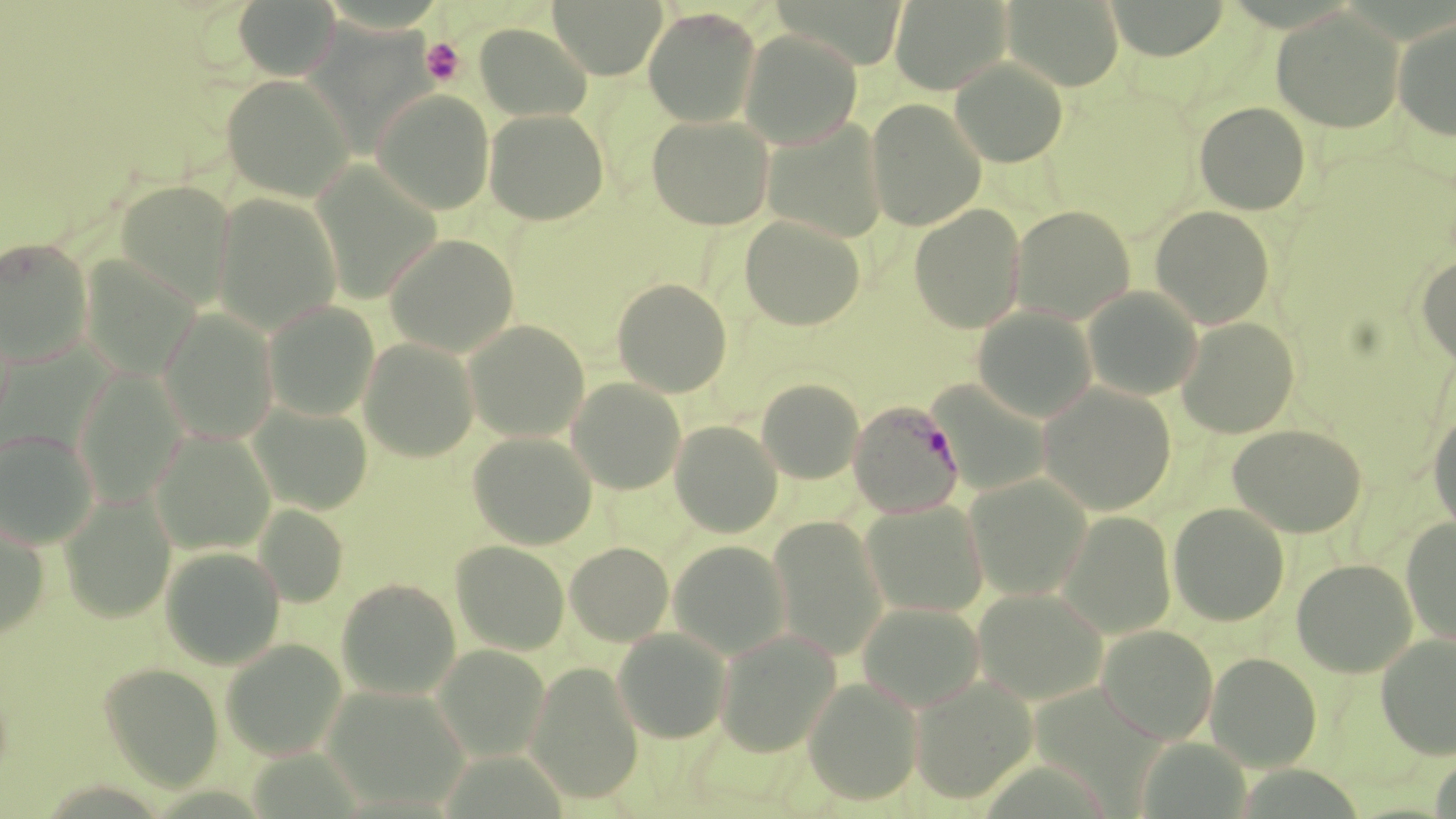
slide-level diagnosis = Plasmodium malariae
stain = May-Grünwald-Giemsa
Plasmodium malariae-infected red blood cell locations = approximate bounding boxes as [x1, y1, x2, y2] in pixels: [848, 400, 964, 518]
field of view = single
magnification = 1000x
modality = optical microscopy
platelet locations = approximate bounding boxes as [x1, y1, x2, y2] in pixels: [421, 38, 465, 86]
image size = 1456×819 pixels
preparation = thin blood film
uninfected red blood cell locations = approximate bounding boxes as [x1, y1, x2, y2] in pixels: [233, 0, 339, 80], [549, 0, 666, 79], [1003, 0, 1125, 90], [1104, 0, 1230, 60], [889, 1, 1011, 95], [643, 7, 762, 128], [1272, 8, 1404, 133], [303, 10, 442, 145], [1393, 16, 1456, 141], [475, 23, 592, 121], [739, 29, 862, 149], [951, 58, 1068, 167], [221, 74, 354, 201], [372, 89, 495, 215], [866, 99, 986, 231], [1194, 102, 1311, 214], [485, 108, 609, 225], [646, 115, 774, 230], [761, 119, 889, 244], [310, 162, 442, 305], [114, 180, 236, 309], [212, 193, 342, 334], [909, 204, 1026, 334], [1010, 205, 1135, 323], [1150, 206, 1275, 329], [739, 214, 866, 331], [385, 233, 520, 357], [0, 237, 94, 366], [1416, 255, 1456, 370], [77, 257, 201, 381], [612, 278, 732, 397], [1082, 286, 1203, 401], [263, 301, 380, 421], [973, 306, 1098, 423], [158, 309, 279, 444], [1176, 316, 1299, 438], [464, 320, 590, 442], [358, 337, 480, 462], [73, 368, 188, 507], [567, 378, 686, 494], [757, 378, 864, 484], [928, 381, 1052, 496], [1038, 384, 1176, 515], [248, 402, 374, 515], [1428, 410, 1456, 534], [670, 420, 783, 538], [1228, 424, 1367, 537], [0, 428, 100, 549], [151, 430, 276, 556], [467, 432, 597, 549], [965, 474, 1093, 600], [59, 490, 176, 623], [859, 500, 990, 619], [1168, 502, 1290, 626], [255, 504, 349, 607], [1056, 511, 1177, 639], [0, 515, 51, 640], [768, 516, 889, 661], [1401, 517, 1456, 647], [451, 540, 570, 655], [668, 540, 792, 659], [565, 542, 674, 646], [160, 545, 285, 669], [1292, 558, 1417, 677], [336, 578, 461, 700], [973, 587, 1108, 705], [858, 601, 985, 712], [1097, 624, 1219, 744], [613, 627, 731, 743], [714, 629, 840, 757], [1376, 632, 1456, 760], [221, 639, 347, 760], [434, 645, 550, 761], [1206, 652, 1322, 771], [100, 661, 224, 793], [525, 661, 645, 805], [910, 676, 1037, 803], [804, 677, 923, 804], [322, 685, 471, 811], [1135, 736, 1252, 819]